Assess this cell for malaria.
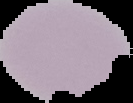
Uninfected.

preparation = thin blood smear
image type = segmented cell region with the area outside set to black
image size = 133×103 pixels